Outline each Plasmodium falciparum-infected red blood cell.
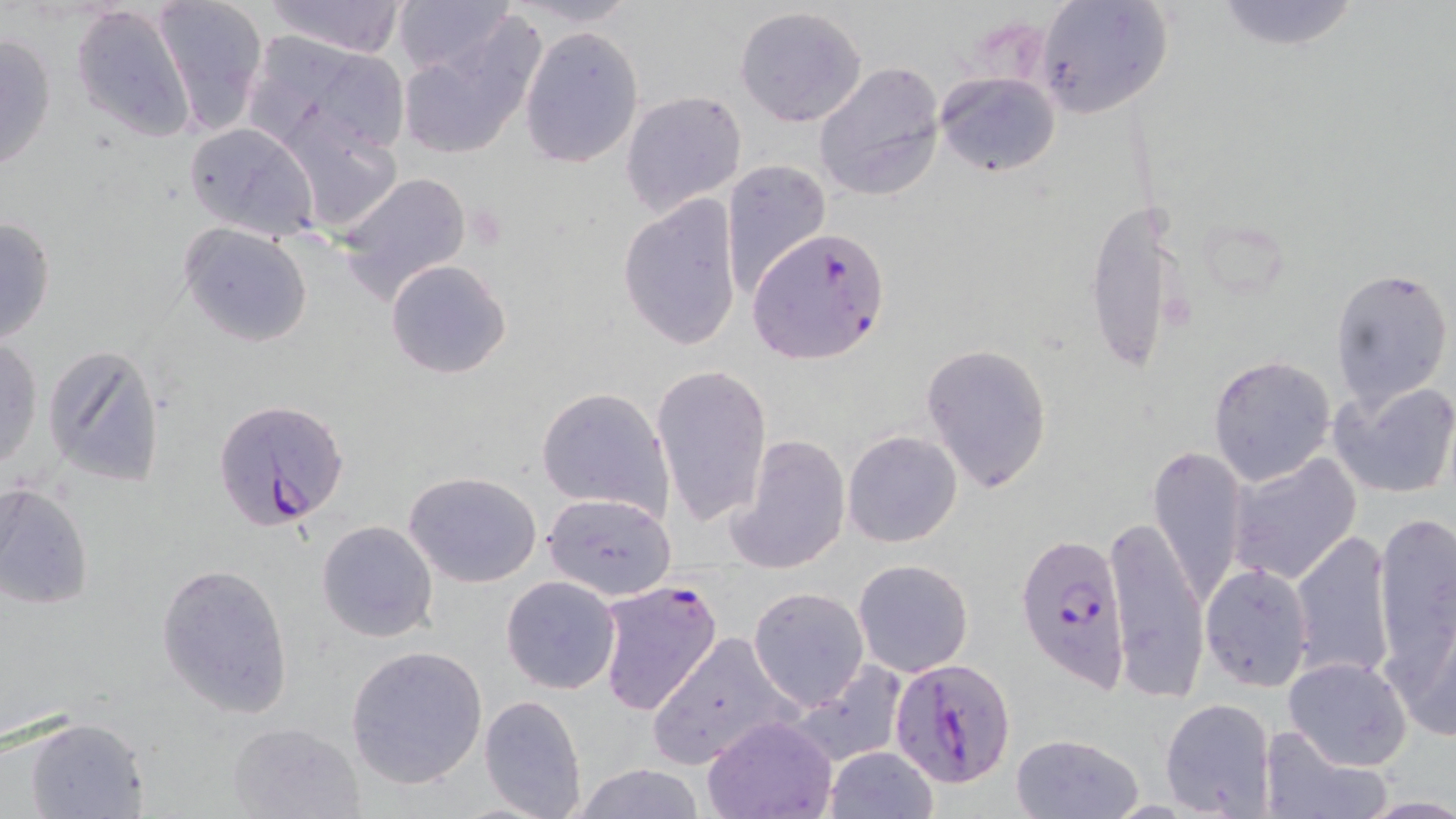
Approximate bounding boxes as (x1, y1, x2, y2) in pixels.
Plasmodium falciparum-infected red blood cells: (749, 226, 892, 365), (211, 397, 351, 534), (1017, 532, 1131, 692), (594, 580, 724, 717), (890, 660, 1018, 787).

slide-level diagnosis = Plasmodium falciparum
field of view = one of a larger specimen
magnification = 1000x
preparation = thin blood smear
image size = 1456×819 pixels
stain = May-Grünwald-Giemsa
modality = light microscopy
uninfected red blood cell locations = approximate bounding boxes as (x1, y1, x2, y2) in pixels: (148, 0, 268, 135), (262, 0, 410, 58), (394, 0, 515, 75), (505, 0, 646, 28), (1206, 0, 1367, 53), (1032, 2, 1173, 120), (69, 4, 198, 143), (734, 6, 868, 127), (395, 20, 544, 162), (519, 25, 645, 168), (1, 29, 58, 174), (239, 29, 413, 156), (813, 60, 946, 201), (936, 70, 1061, 178), (621, 90, 748, 217), (284, 113, 406, 235), (184, 121, 318, 243), (720, 159, 831, 296), (336, 170, 474, 303), (617, 194, 743, 350), (1083, 200, 1188, 381), (0, 214, 57, 348), (178, 224, 314, 348), (385, 259, 512, 379), (1330, 264, 1454, 408), (0, 337, 44, 470), (921, 342, 1053, 493), (40, 343, 167, 488), (1206, 355, 1337, 488), (652, 363, 772, 528), (1330, 378, 1456, 499), (536, 386, 674, 521), (843, 430, 963, 548), (727, 433, 851, 574), (1147, 445, 1247, 605), (1226, 451, 1362, 586), (403, 471, 545, 589), (0, 481, 95, 611), (544, 489, 670, 599), (1373, 511, 1455, 665), (1105, 514, 1209, 697), (316, 520, 437, 643), (1289, 528, 1398, 684), (852, 558, 974, 678), (156, 560, 295, 718), (1201, 563, 1315, 690), (500, 575, 622, 694), (747, 586, 870, 710), (1391, 600, 1456, 744), (647, 632, 797, 770), (345, 644, 488, 789), (1283, 656, 1412, 771), (788, 659, 907, 767), (479, 694, 587, 819), (1160, 697, 1278, 817), (701, 714, 839, 819), (21, 717, 150, 819), (225, 720, 367, 819), (1258, 724, 1390, 819), (1010, 732, 1142, 818), (825, 746, 938, 818), (569, 763, 708, 819), (1360, 796, 1456, 817)